Report the malaria status of this cell.
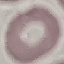

It is uninfected.

Summary:
  - Stain: Giemsa
  - Capture: smartphone camera at the microscope eyepiece
  - Image type: cell patch, automatically extracted from a larger field of view and resized to 64 × 64 pixels
  - Preparation: thin blood smear